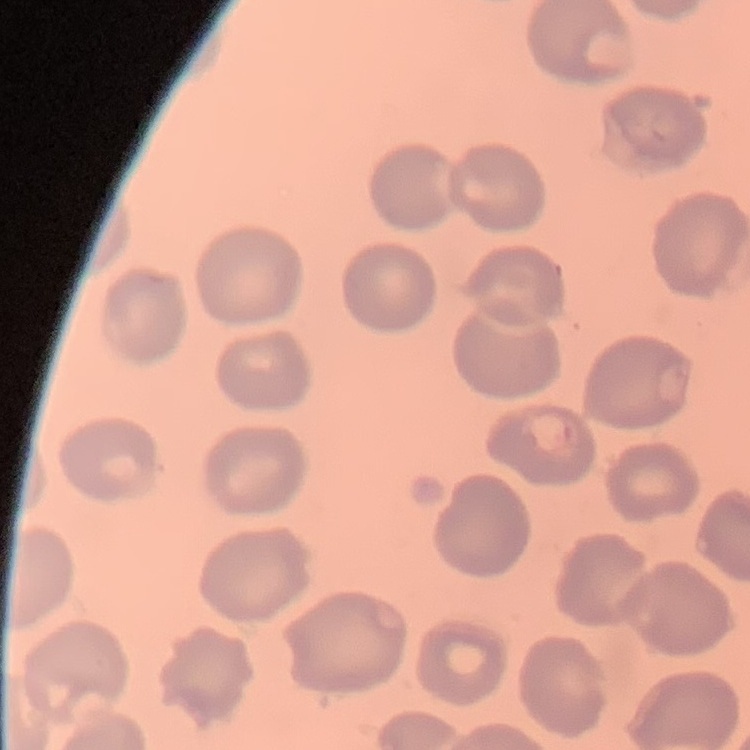

erythrocyte morphology = no rouleaux formation
preparation = thin peripheral smear
image type = one tile cut from a larger photomicrograph
stain = Field's or Giemsa